Name the cell type shown.
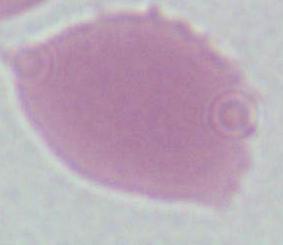
This is an erythrocyte.

modality = photomicrograph
magnification = 1000x